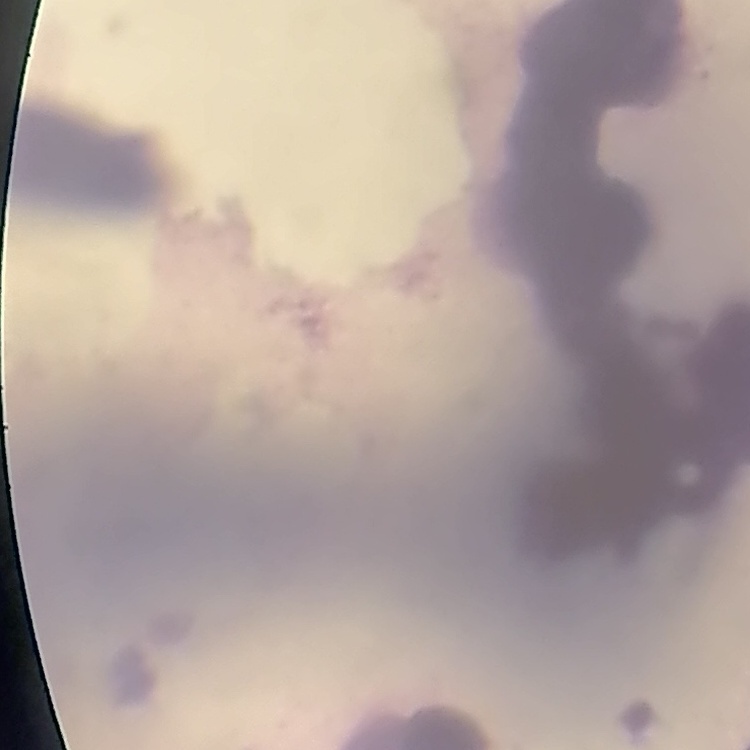

Summary:
  - Red blood cell morphology: rouleaux formation
  - Image type: one tile cut from a larger photomicrograph
  - Stain: Field's or Giemsa
  - Preparation: thin blood film